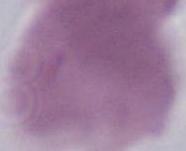

identification = erythrocyte
magnification = 1000x
modality = photomicrograph